Identify the parasite.
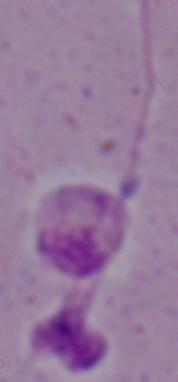
Leishmania.

modality: photomicrograph
magnification: 1000x